Assess the morphology of the erythrocytes.
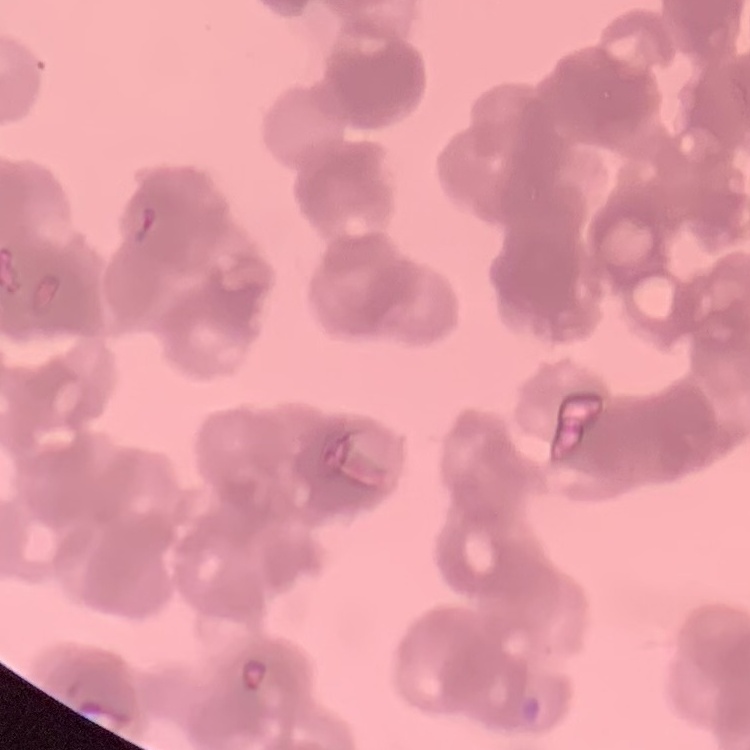
They show rouleaux formation.

preparation = thin blood smear
stain = Field's or Giemsa
image type = square crop of a larger photomicrograph